Give the position of every leukocyte visible.
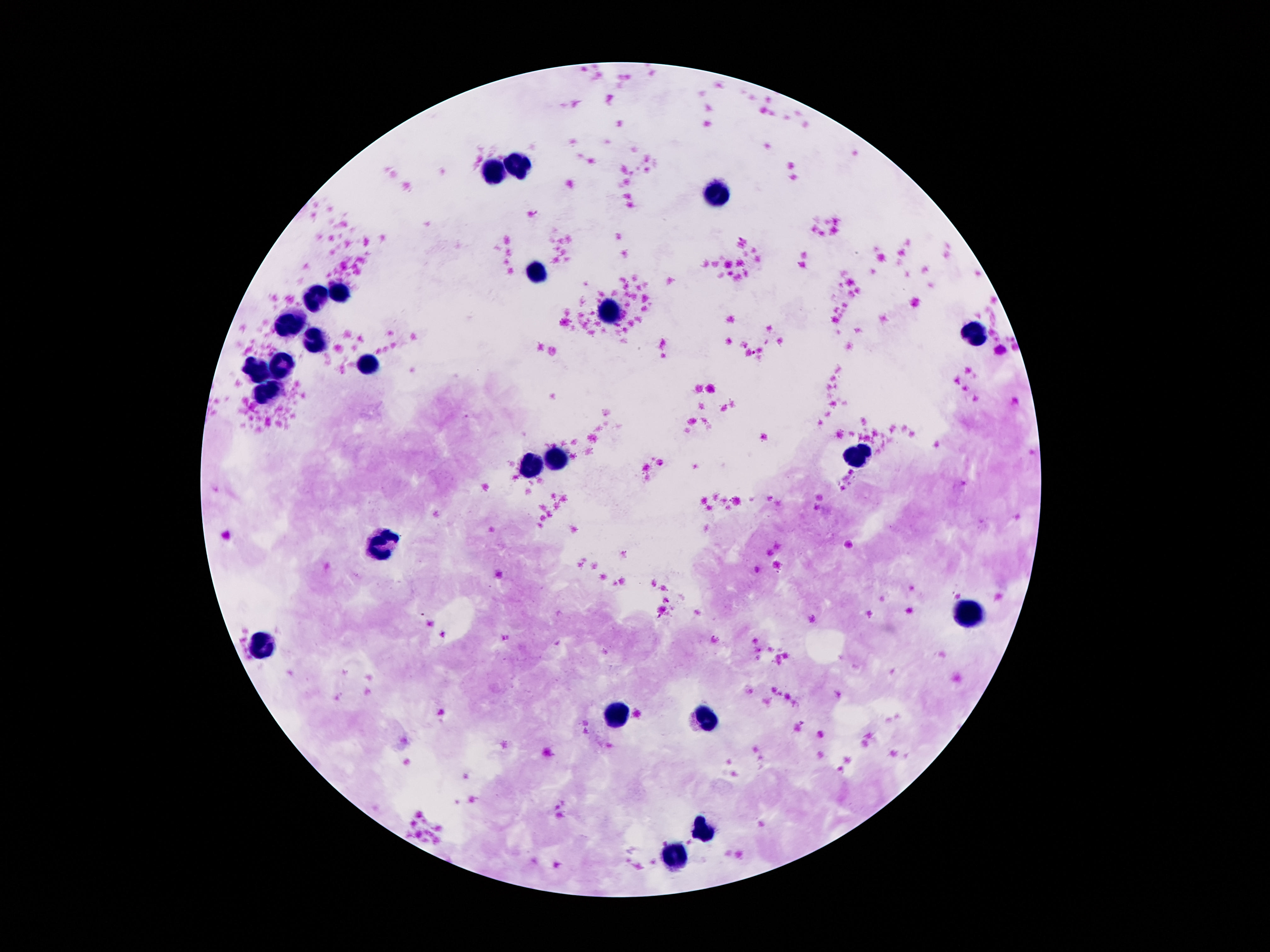
Approximate object centers, in pixels from the top-left corner.
Leukocytes: (x=494, y=169), (x=518, y=169), (x=722, y=197), (x=537, y=274), (x=319, y=292), (x=339, y=294), (x=610, y=316), (x=292, y=324), (x=976, y=335), (x=315, y=342), (x=283, y=363), (x=371, y=365), (x=257, y=372), (x=266, y=395), (x=858, y=452), (x=559, y=460), (x=533, y=467), (x=384, y=547), (x=968, y=611), (x=266, y=644), (x=617, y=715), (x=703, y=716), (x=703, y=828), (x=673, y=856).

Summary:
  - Stain: Giemsa
  - Image size: 1270×952 pixels
  - Patient malaria status: negative
  - Magnification: 100x
  - Capture: smartphone camera through the microscope eyepiece
  - Field of view: single
  - Preparation: thick blood smear